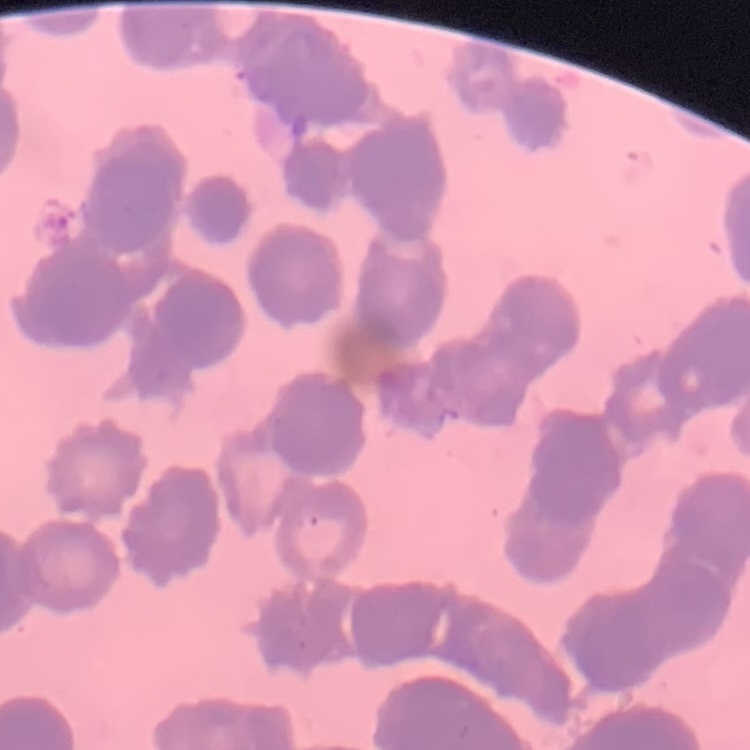

red blood cell morphology = rouleaux formation
image type = one tile cut from a larger photomicrograph
preparation = thin blood smear
stain = Field's or Giemsa